Assess this cell for malaria.
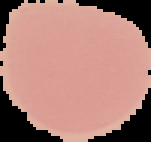

It is uninfected.

{
  "image_type": "segmented cell region on a black background",
  "preparation": "thin blood film",
  "image_size": "151×142 pixels"
}